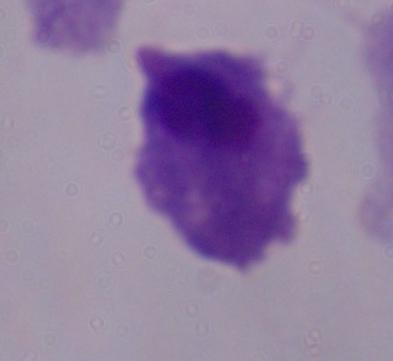
1000x magnification. A trichomonad is shown. Micrograph.